Report the malaria status of this cell.
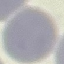
Uninfected.

Thin blood smear. Giemsa stain. Photographed with a smartphone camera at the microscope eyepiece. Automatically extracted cell patch, resized to 64 × 64 pixels.